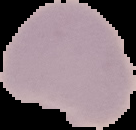
Summary:
  - Image size: 136×130 pixels
  - Preparation: thin blood film
  - Image type: segmented cell region on a black background
  - Result: no malaria parasites detected